State which parasite is depicted.
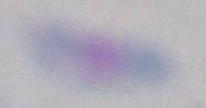

This is Toxoplasma gondii.

Photomicrograph. 1000x magnification.